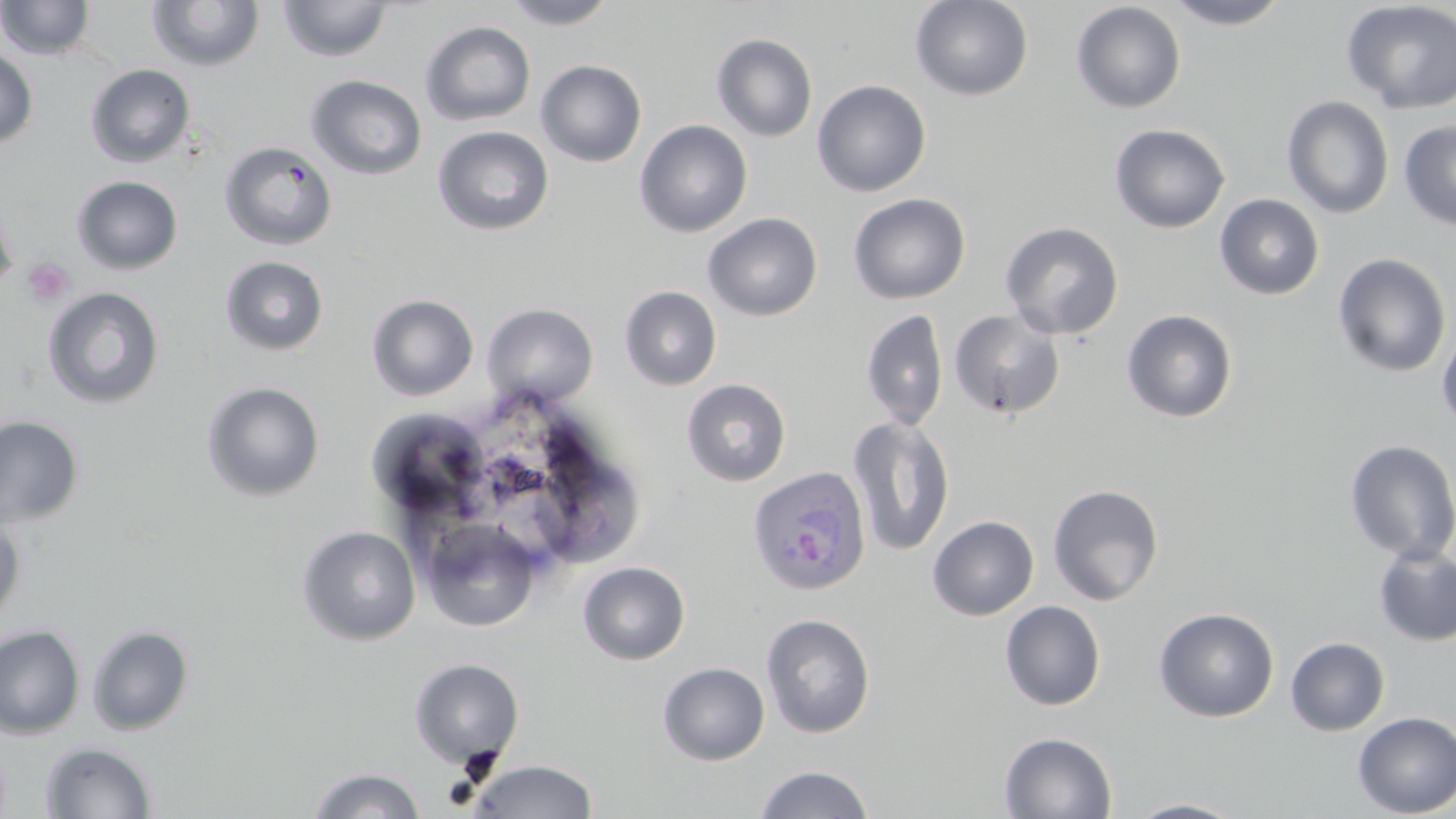

Approximate bounding boxes as (x1,y1)-(x2,y2) corner pairs in pixels. Platelet locations: (22,258)-(73,307). Uninfected red blood cell locations: (0,0)-(97,60), (278,0)-(392,62), (502,0)-(619,29), (910,0)-(1034,101), (1164,0)-(1293,29), (146,1)-(265,72), (1341,1)-(1456,114), (1070,2)-(1186,114), (420,21)-(536,126), (712,34)-(817,142), (0,47)-(38,149), (535,60)-(647,167), (86,64)-(196,167), (306,74)-(428,180), (812,79)-(932,197), (1282,96)-(1394,218), (634,119)-(753,237), (1398,120)-(1456,231), (1110,123)-(1230,233), (432,125)-(554,235), (219,141)-(337,250), (72,175)-(183,274), (0,192)-(18,296), (854,192)-(957,433), (848,193)-(971,304), (1214,194)-(1325,299), (703,212)-(823,321), (1000,221)-(1124,339), (1332,253)-(1452,378), (221,256)-(329,355), (619,286)-(722,391), (43,287)-(165,408), (367,294)-(479,401), (481,303)-(598,407), (860,309)-(949,431), (948,309)-(1066,419), (1121,309)-(1238,423), (1436,324)-(1456,434), (681,378)-(791,487), (201,381)-(325,501), (362,415)-(485,514), (0,416)-(83,527), (847,416)-(955,557), (1344,439)-(1456,562), (530,452)-(653,565), (1047,484)-(1163,606), (0,512)-(25,631), (927,515)-(1039,620), (420,517)-(541,633), (296,525)-(421,645), (1373,544)-(1456,647), (577,561)-(690,665), (1000,600)-(1106,711), (1153,607)-(1279,722), (760,613)-(876,738), (0,624)-(86,740), (87,624)-(194,735), (1285,636)-(1390,736), (409,658)-(524,768), (658,662)-(769,765), (1353,711)-(1456,817), (999,732)-(1117,818), (41,742)-(157,818), (466,759)-(599,818), (754,765)-(874,819), (309,767)-(425,818), (1126,798)-(1247,818). Plasmodium ovale-infected red blood cell locations: (746,466)-(873,596). Slide-level diagnosis: Plasmodium ovale. May-Grünwald-Giemsa stain. Thin blood film. 1000x magnification. Light microscopy. One field of a larger specimen. Image is 1456×819 pixels.